Name the parasite shown.
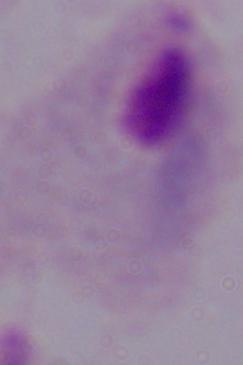
A trichomonad.

Summary:
  - Modality: photomicrograph
  - Magnification: 1000x